Look for Plasmodium parasites.
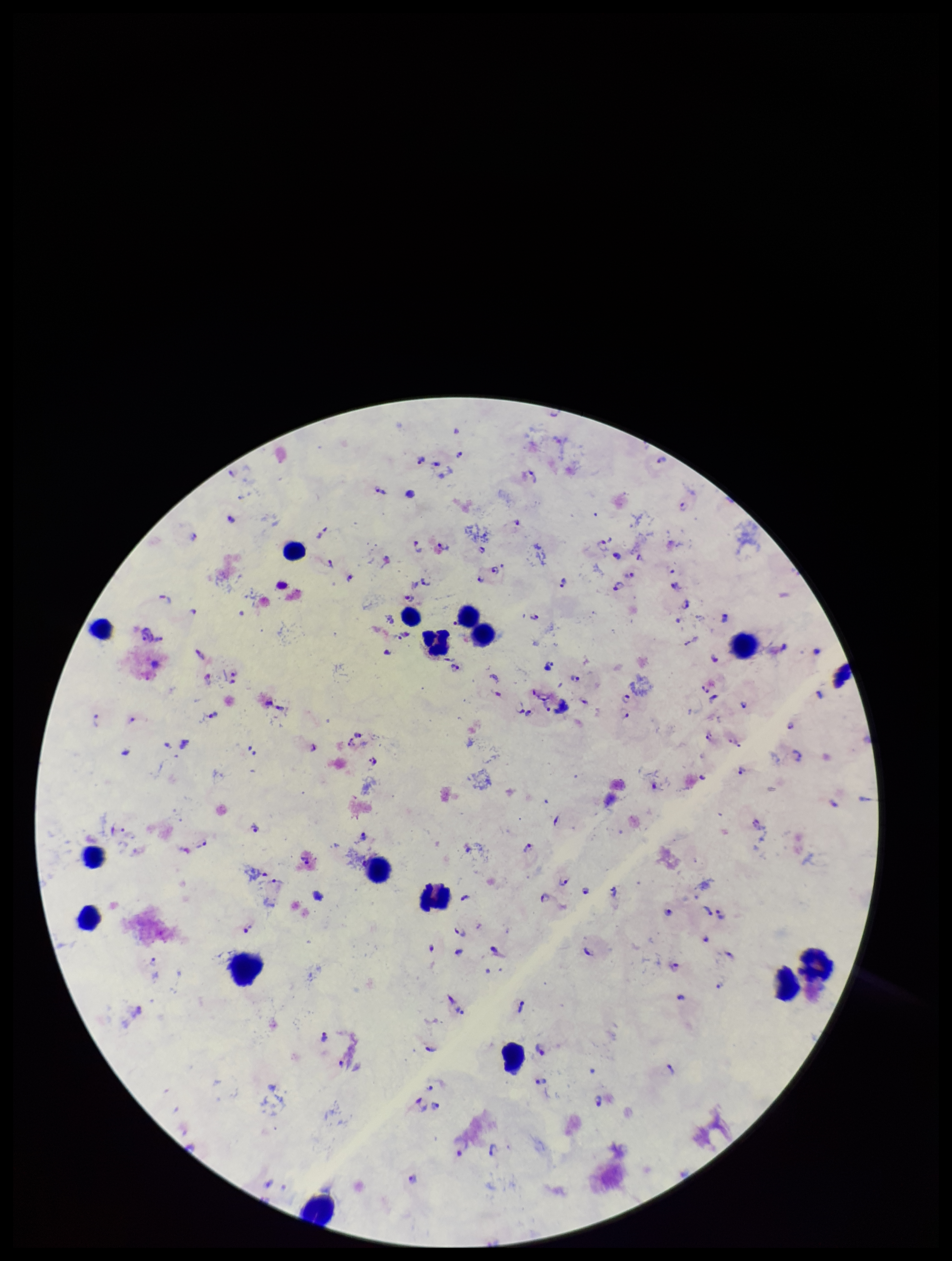
Detected.

Photographed through the microscope eyepiece with a smartphone camera. Preparation: thick smear. Image is 952×1261 pixels. Stained with Giemsa. Single field of view. Species reported for this patient: Plasmodium falciparum. Patient malaria status: infected. Parasite count: 100. Leukocyte count: 18.